Outline each blood parasite and name the species.
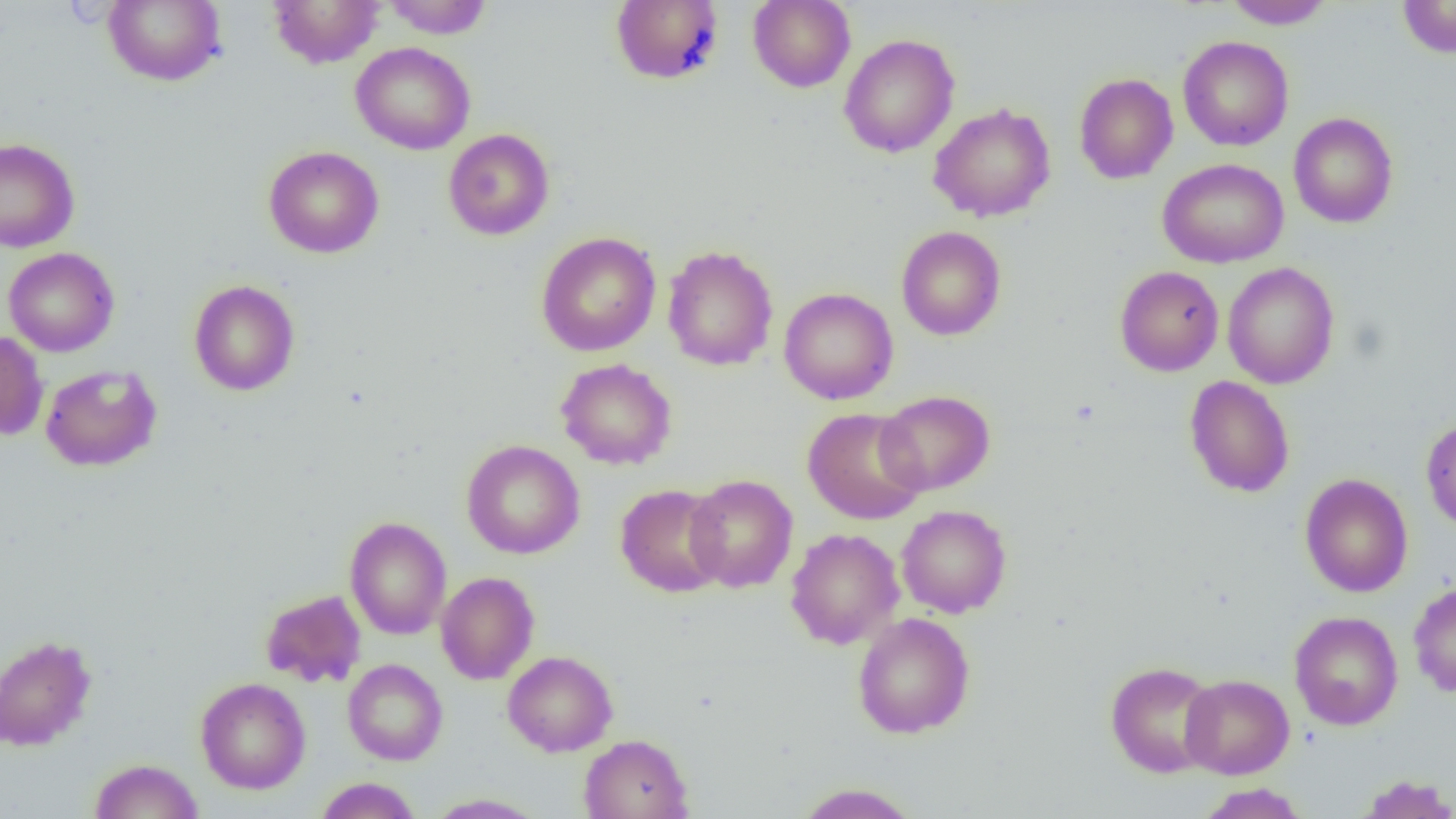
No blood parasites observed.

Summary:
  - Coordinate format: approximate bounding boxes as named x1/y1/x2/y2 corners in pixels
  - Uninfected red blood cell locations: (x1=103, y1=0, x2=226, y2=87), (x1=268, y1=0, x2=384, y2=68), (x1=383, y1=0, x2=492, y2=38), (x1=748, y1=0, x2=855, y2=92), (x1=1224, y1=0, x2=1334, y2=29), (x1=1397, y1=0, x2=1456, y2=58), (x1=610, y1=1, x2=725, y2=85), (x1=839, y1=33, x2=960, y2=158), (x1=1178, y1=35, x2=1293, y2=151), (x1=350, y1=41, x2=476, y2=155), (x1=1074, y1=72, x2=1178, y2=184), (x1=928, y1=102, x2=1056, y2=222), (x1=1288, y1=112, x2=1398, y2=228), (x1=443, y1=128, x2=555, y2=240), (x1=0, y1=138, x2=80, y2=252), (x1=263, y1=145, x2=384, y2=258), (x1=1157, y1=158, x2=1289, y2=268), (x1=896, y1=226, x2=1006, y2=341), (x1=536, y1=232, x2=661, y2=356), (x1=662, y1=245, x2=778, y2=371), (x1=4, y1=247, x2=119, y2=357), (x1=1222, y1=262, x2=1340, y2=389), (x1=1114, y1=265, x2=1224, y2=376), (x1=188, y1=279, x2=300, y2=395), (x1=779, y1=287, x2=899, y2=405), (x1=0, y1=331, x2=49, y2=441), (x1=556, y1=358, x2=677, y2=470), (x1=40, y1=364, x2=163, y2=472), (x1=1184, y1=376, x2=1295, y2=498), (x1=876, y1=390, x2=995, y2=495), (x1=803, y1=407, x2=927, y2=524), (x1=1420, y1=417, x2=1456, y2=531), (x1=461, y1=440, x2=585, y2=559), (x1=1299, y1=473, x2=1413, y2=598), (x1=685, y1=474, x2=798, y2=592), (x1=615, y1=484, x2=729, y2=597), (x1=896, y1=505, x2=1012, y2=618), (x1=344, y1=516, x2=451, y2=640), (x1=786, y1=528, x2=904, y2=649), (x1=436, y1=571, x2=540, y2=684), (x1=1408, y1=582, x2=1456, y2=698), (x1=260, y1=589, x2=367, y2=688), (x1=1288, y1=611, x2=1403, y2=730), (x1=852, y1=612, x2=975, y2=739), (x1=0, y1=634, x2=97, y2=751), (x1=502, y1=651, x2=618, y2=756), (x1=343, y1=659, x2=448, y2=765), (x1=1105, y1=660, x2=1220, y2=778), (x1=1179, y1=674, x2=1294, y2=779), (x1=195, y1=677, x2=311, y2=794), (x1=579, y1=734, x2=693, y2=819), (x1=89, y1=758, x2=203, y2=818), (x1=1356, y1=774, x2=1456, y2=818), (x1=314, y1=777, x2=421, y2=818), (x1=794, y1=783, x2=921, y2=819), (x1=1195, y1=783, x2=1311, y2=818), (x1=424, y1=793, x2=548, y2=818)
  - Slide-level diagnosis: no evidence of blood parasites
  - Image size: 1456×819 pixels
  - Magnification: 1000x
  - Field of view: single
  - Preparation: thin blood film
  - Modality: optical microscopy